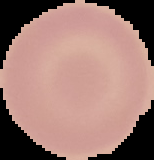
The area outside the segmented cell region is set to black. Malaria status: uninfected. From a thin blood film. Image is 154×160 pixels.